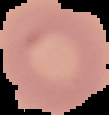 From a thin blood film. Image is 109×115 pixels. Malaria status: uninfected. Cell region segmented out of the field of view; the surrounding area is masked to black.